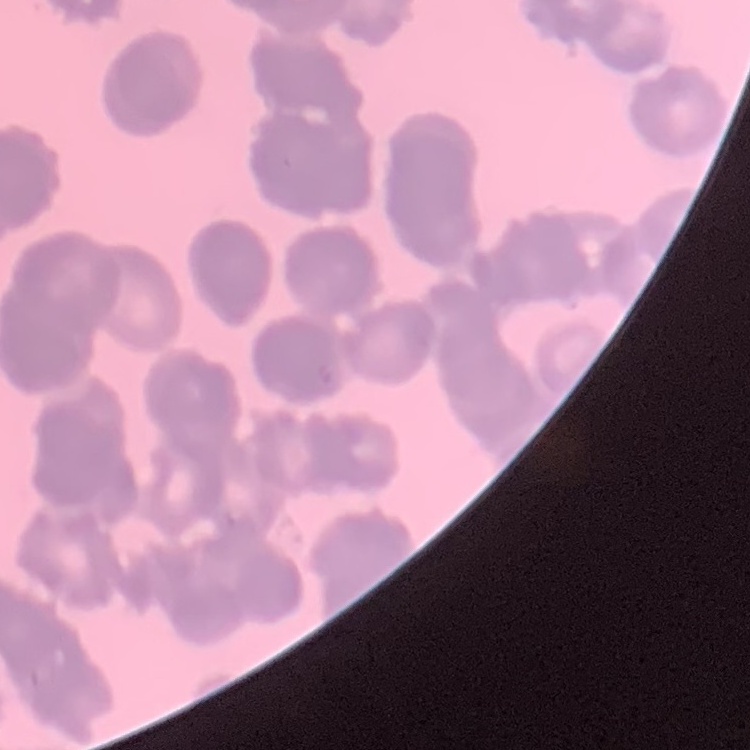

Summary:
  - Erythrocyte morphology: rouleaux formation
  - Preparation: thin peripheral smear
  - Stain: Field's or Giemsa
  - Image type: square crop of a larger photomicrograph